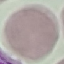

result = negative for malaria parasites
image type = automatically extracted cell patch, resized to 64 × 64 pixels
stain = Giemsa
preparation = thin blood film
capture = smartphone camera at the microscope eyepiece